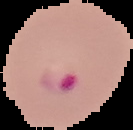

Summary:
  - Image type: segmented cell region on a black background
  - Malaria status: parasitized
  - Preparation: thin blood film
  - Image size: 133×130 pixels